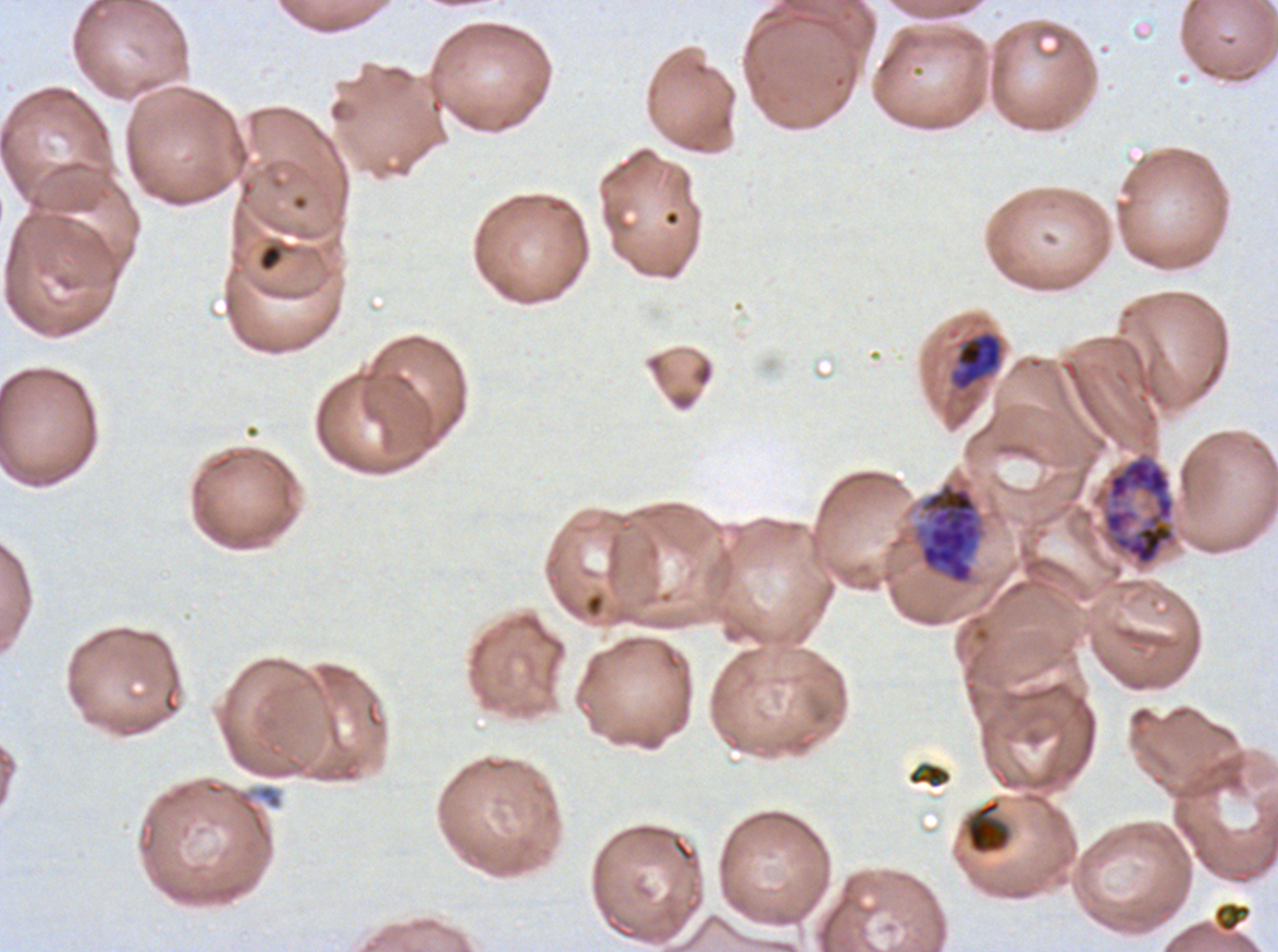
Approximate bounding boxes as (x1, y1, x2, y2) in pixels.
Summary:
  - Debris locations: (258, 243, 283, 272), (907, 763, 952, 789), (965, 798, 1012, 855), (1212, 901, 1252, 934)
  - Mid trophozoite locations: (950, 331, 1002, 391)
  - Early schizont locations: (1101, 452, 1177, 567), (911, 480, 988, 586)
  - Specimen: P. falciparum from a patient in The Gambia, cultured ex vivo for 24 to 48 hours
  - Field of view: one sub-image of a larger composite
  - Stain: Giemsa
  - Image size: 1278×952 pixels
  - Preparation: thin blood film
  - Life-cycle stages observed: mid trophozoite, early schizont